Name the parasite shown.
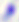
This is Toxoplasma gondii.

modality: photomicrograph
magnification: 400x